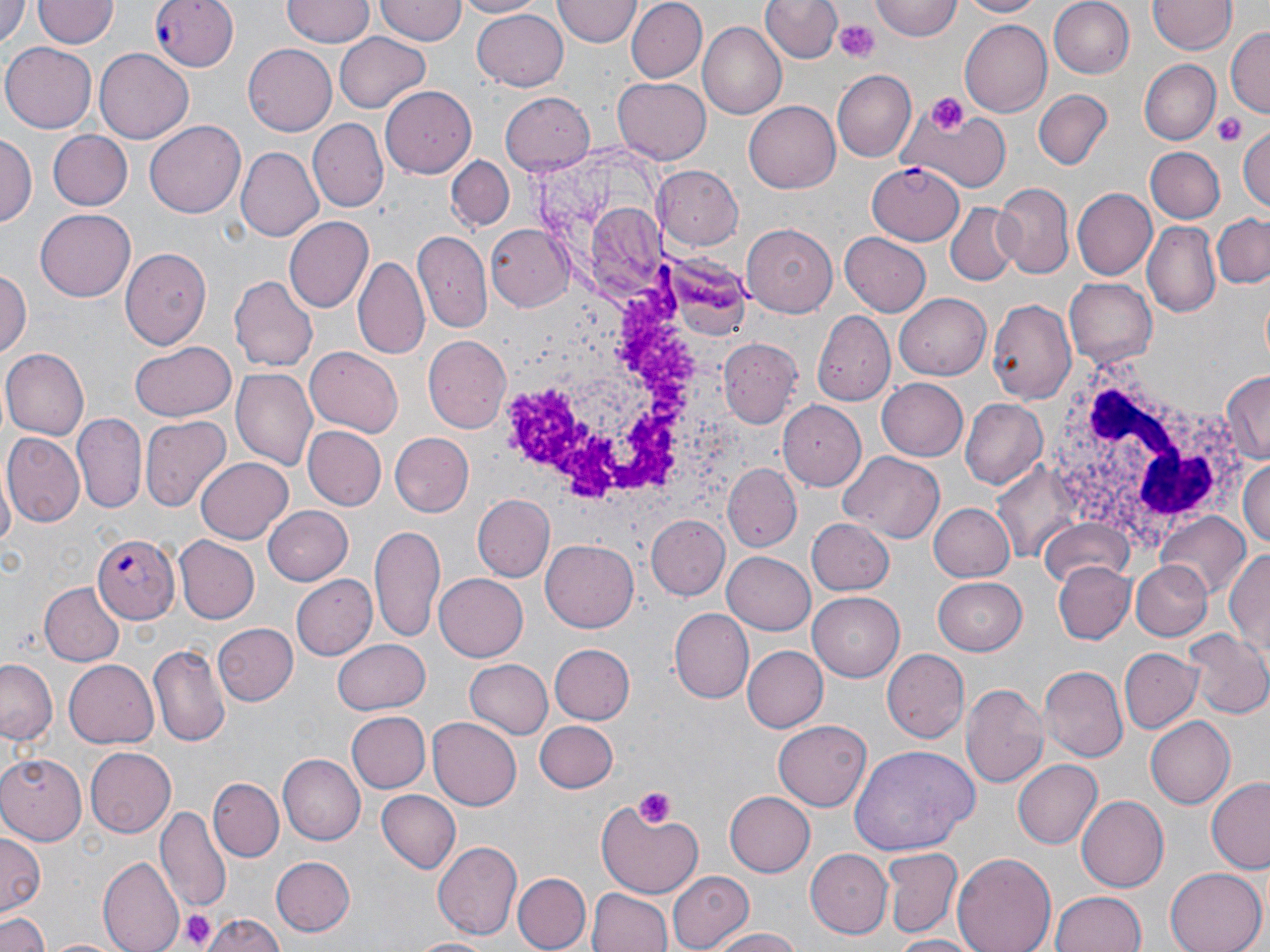

Summary:
  - Coordinate format: approximate bounding boxes as [x1, y1, x2, y2] in pixels
  - Platelet locations: [835, 20, 880, 63], [923, 93, 968, 133], [1210, 110, 1248, 148], [633, 786, 676, 829], [177, 908, 217, 951]
  - Plasmodium falciparum-infected red blood cell locations (subset): [151, 0, 241, 73], [866, 161, 963, 244], [94, 531, 180, 623]
  - White blood cell locations: [503, 260, 706, 512], [1041, 362, 1251, 563]
  - Uninfected red blood cell locations (subset): [0, 0, 29, 47], [36, 0, 116, 50], [281, 0, 373, 46], [454, 0, 546, 18], [571, 0, 690, 56], [624, 0, 705, 83], [761, 0, 841, 64], [870, 0, 960, 41], [960, 0, 1046, 18], [1048, 0, 1135, 80], [375, 1, 466, 45], [552, 1, 640, 47], [1150, 1, 1234, 55], [471, 6, 568, 91], [960, 20, 1052, 116], [697, 22, 786, 119], [1227, 28, 1268, 118], [333, 32, 431, 114], [3, 41, 99, 133], [243, 45, 337, 137], [96, 49, 194, 143], [1139, 60, 1218, 143], [833, 70, 918, 164], [612, 76, 710, 163], [381, 86, 478, 177], [1034, 89, 1112, 169], [503, 93, 593, 174], [744, 99, 843, 193], [909, 104, 1009, 193], [309, 119, 386, 210], [145, 120, 246, 217], [1237, 127, 1269, 211], [45, 130, 133, 211], [1, 134, 34, 227], [1145, 146, 1224, 224], [235, 149, 323, 242], [446, 157, 515, 232], [653, 166, 744, 250], [997, 182, 1073, 279], [1073, 188, 1157, 279], [946, 203, 1019, 285], [35, 210, 136, 302], [1209, 213, 1270, 290], [283, 217, 372, 313], [1143, 220, 1221, 317], [741, 222, 840, 313], [486, 224, 574, 313], [839, 232, 931, 316], [412, 233, 492, 334], [120, 247, 211, 347], [354, 258, 429, 363], [0, 269, 30, 359], [230, 276, 318, 370], [1063, 276, 1158, 367], [895, 294, 991, 380], [988, 299, 1078, 404], [812, 311, 894, 403], [422, 336, 511, 434], [718, 340, 799, 429], [129, 342, 237, 421], [305, 347, 403, 438], [2, 349, 89, 438], [232, 370, 319, 473], [1221, 370, 1270, 466], [876, 377, 969, 462], [961, 397, 1047, 488], [73, 412, 147, 512], [140, 415, 231, 512], [303, 425, 387, 510], [390, 432, 474, 517], [4, 433, 84, 524], [841, 451, 945, 544], [196, 455, 294, 542], [1241, 456, 1270, 552], [723, 466, 802, 552], [1, 474, 15, 560], [472, 495, 554, 581], [930, 502, 1017, 582], [263, 505, 355, 582], [1156, 512, 1252, 598], [648, 516, 729, 599], [804, 517, 893, 596], [1037, 519, 1135, 591], [371, 525, 447, 644], [175, 537, 257, 622], [541, 540, 637, 632], [1227, 544, 1270, 660], [722, 551, 816, 635], [1129, 559, 1212, 642], [1055, 564, 1133, 644], [434, 574, 528, 662], [932, 575, 1028, 654], [293, 576, 377, 659], [42, 582, 124, 666], [807, 592, 907, 682], [669, 609, 752, 705], [212, 623, 298, 707], [1186, 631, 1269, 721], [330, 639, 431, 714], [549, 643, 634, 725], [148, 644, 231, 749], [741, 645, 827, 734], [1119, 647, 1200, 735], [882, 649, 969, 744], [1, 657, 59, 747], [65, 657, 161, 748], [466, 658, 552, 740], [1041, 664, 1129, 762], [961, 685, 1050, 789], [346, 710, 430, 793], [427, 716, 523, 809], [1146, 717, 1236, 808], [534, 721, 618, 792], [774, 721, 872, 810], [85, 747, 176, 837], [853, 747, 977, 856], [279, 754, 365, 843], [0, 755, 85, 842], [1012, 759, 1101, 850], [1207, 778, 1270, 872], [208, 779, 283, 863], [376, 790, 462, 875], [723, 790, 815, 877], [1077, 796, 1168, 891], [596, 798, 704, 898], [157, 806, 230, 910], [0, 832, 43, 913], [431, 841, 523, 939], [882, 847, 961, 937], [804, 849, 892, 939], [952, 852, 1057, 952], [98, 856, 182, 952], [270, 856, 354, 936], [1165, 867, 1266, 952], [667, 870, 755, 952], [512, 873, 588, 952], [588, 888, 671, 952], [1049, 890, 1149, 952], [203, 912, 286, 952], [0, 913, 50, 952], [708, 928, 804, 952], [886, 934, 979, 951], [411, 936, 496, 952], [43, 937, 128, 952]
  - Slide-level diagnosis: Plasmodium falciparum
  - Image size: 1270×952 pixels
  - Modality: light microscopy
  - Magnification: 1000x
  - Preparation: thin blood smear
  - Stain: May-Grünwald-Giemsa
  - Field of view: one of a larger specimen